Give the position of every leukocyte visible.
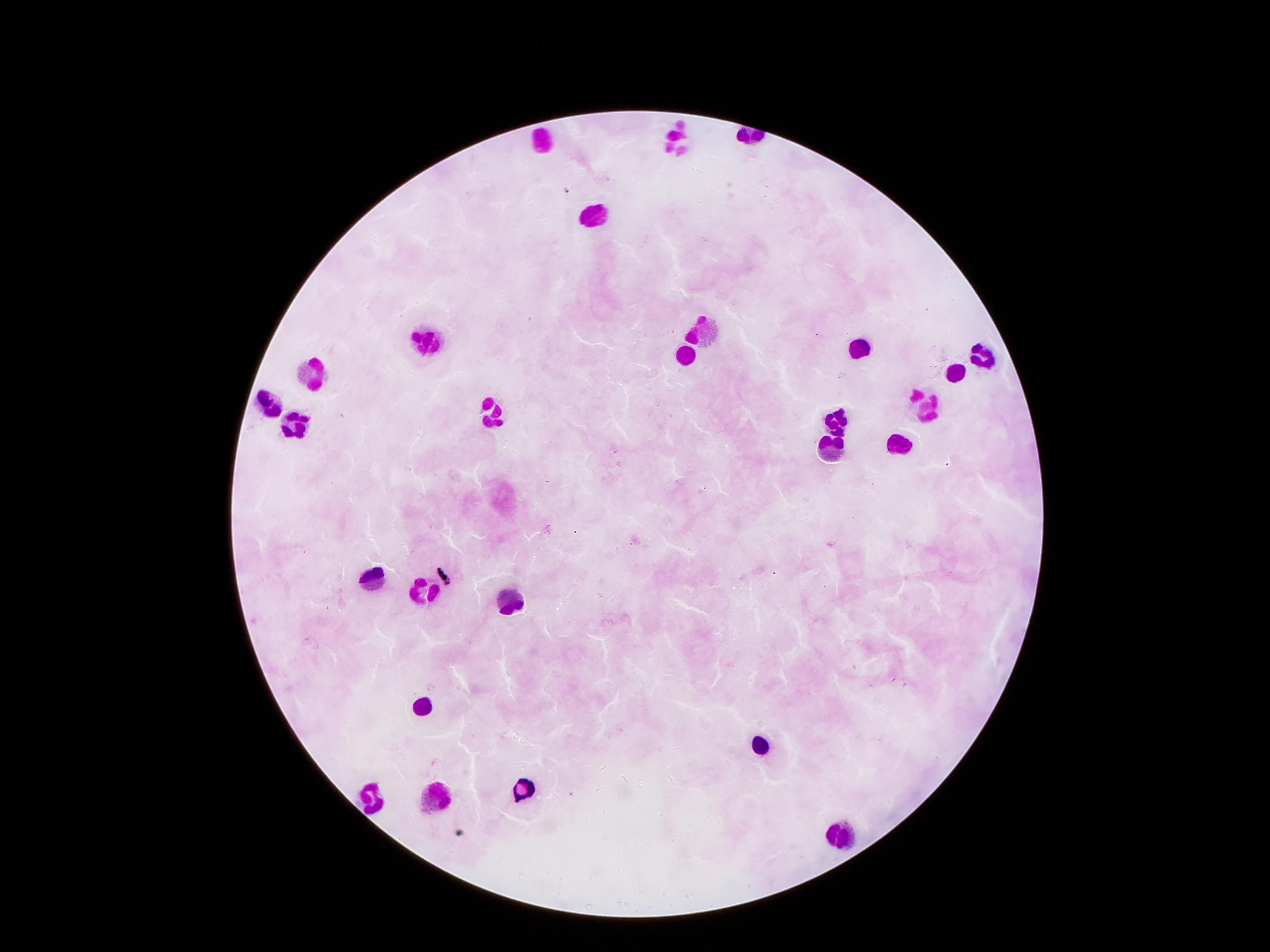

Approximate centers as [x, y] in pixels.
Leukocytes: [543, 137], [674, 137], [600, 214], [707, 329], [431, 338], [858, 349], [980, 351], [685, 355], [311, 370], [953, 370], [267, 406], [925, 406], [490, 413], [836, 418], [296, 427], [898, 438], [831, 454], [371, 578], [423, 593], [510, 600], [424, 706], [758, 746], [522, 788], [436, 793], [371, 794], [843, 835].

Single field of view. Image is 1270×952 pixels. Patient malaria status: uninfected. Giemsa-stained preparation. Photographed through the microscope eyepiece with a smartphone camera. 100x magnification. Thick peripheral-blood smear.